Assess this cell for malaria.
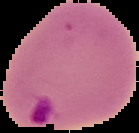
Parasitized.

The area outside the segmented cell region is set to black. From a thin blood smear. Image is 139×133 pixels.